Report the malaria status of this cell.
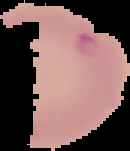

Parasitized.

Summary:
  - Image type: segmented cell region with the area outside set to black
  - Preparation: thin blood film
  - Image size: 130×151 pixels